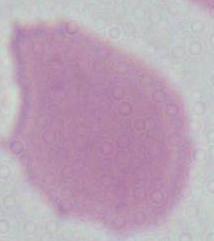

identification = red blood cell
modality = micrograph
magnification = 1000x